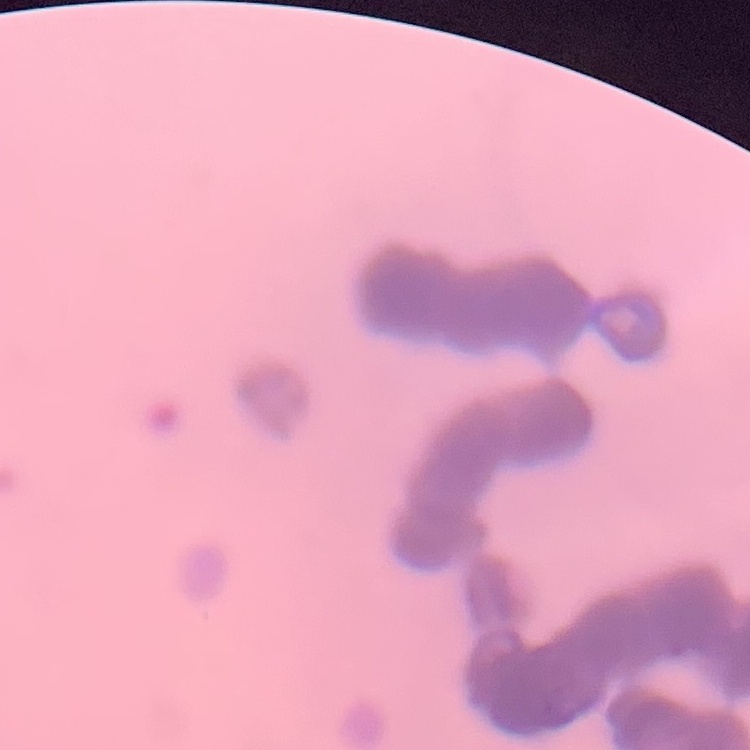 The red blood cells show rouleaux formation. Stained with either Field's or Giemsa. Thin blood film. Square crop of a larger photomicrograph.